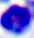
Summary:
  - Magnification: 400x
  - Modality: photomicrograph
  - Identification: white blood cell